State which parasite is depicted.
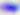
This is Toxoplasma gondii.

400x magnification. Photomicrograph.